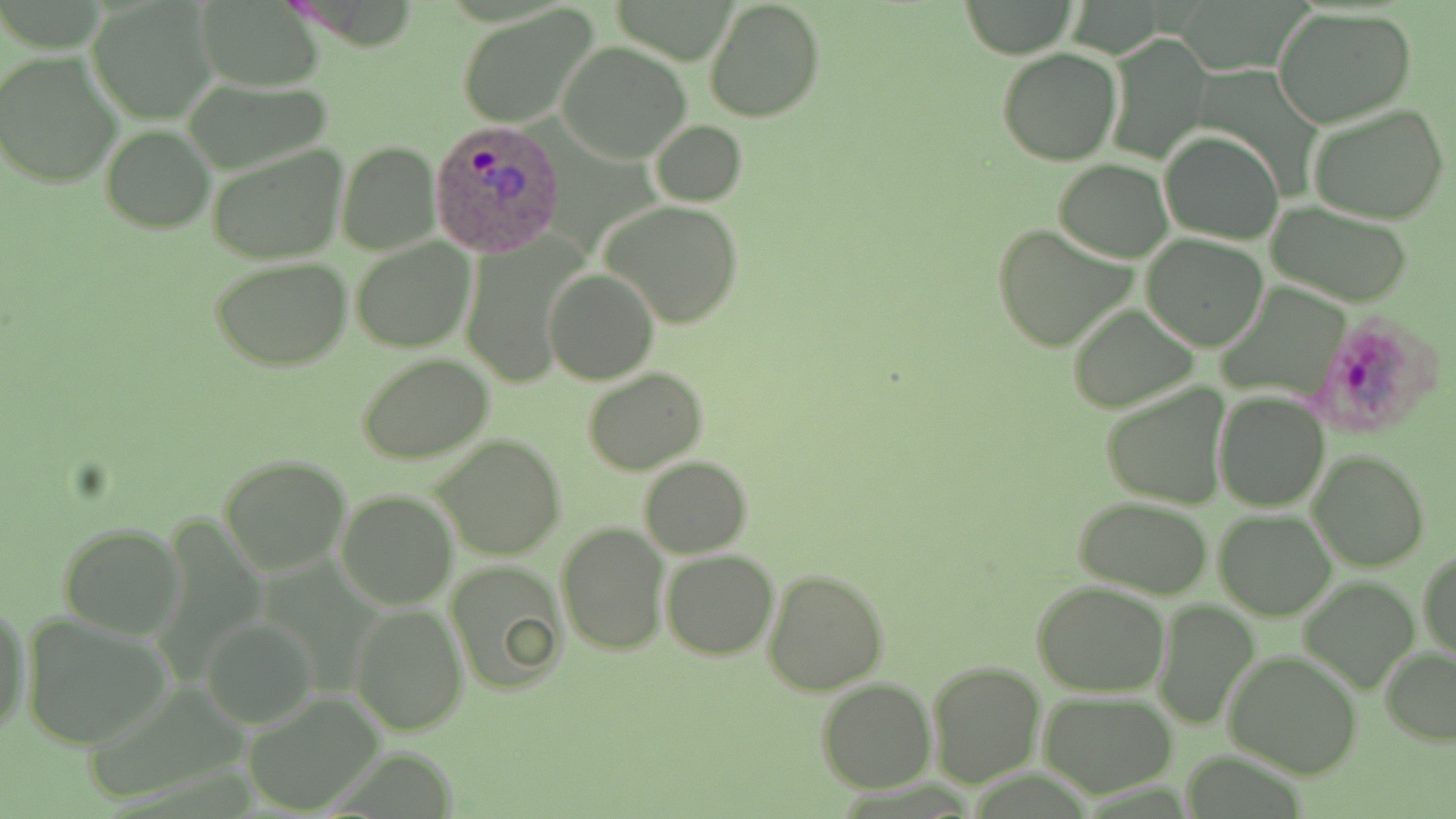
Summary:
  - Coordinate format: approximate bounding boxes as (x1,y1)-(x2,y2) corner pairs in pixels
  - Uninfected red blood cell locations: (87,0)-(219,122), (702,0)-(826,123), (193,1)-(328,90), (961,1)-(1077,58), (456,6)-(599,128), (1272,7)-(1417,128), (1103,33)-(1211,163), (558,41)-(694,165), (997,48)-(1121,165), (1,52)-(123,188), (183,76)-(339,177), (1308,103)-(1449,224), (649,119)-(747,206), (100,125)-(214,233), (1160,130)-(1284,244), (337,142)-(440,255), (206,145)-(349,263), (1055,159)-(1170,261), (336,167)-(450,323), (602,200)-(744,328), (1265,202)-(1415,306), (992,224)-(1138,353), (457,234)-(588,390), (1142,236)-(1270,351), (350,238)-(475,352), (209,256)-(354,370), (543,268)-(661,385), (1067,304)-(1199,414), (355,353)-(495,466), (582,365)-(708,475), (1103,385)-(1227,507), (1213,391)-(1329,512), (432,434)-(566,559), (1309,450)-(1431,572), (219,455)-(350,575), (639,457)-(752,558), (335,488)-(457,610), (1075,498)-(1213,599), (1213,509)-(1337,621), (556,522)-(668,655), (58,523)-(183,636), (662,548)-(779,660), (1418,548)-(1455,665), (444,560)-(568,695), (762,568)-(889,697), (1300,576)-(1420,694), (1033,580)-(1169,698), (1155,601)-(1259,731), (0,602)-(30,742), (350,605)-(468,735), (20,612)-(174,748), (203,618)-(317,731), (1380,647)-(1455,745), (1225,648)-(1364,778), (927,659)-(1046,786), (815,678)-(936,794), (1040,691)-(1179,798), (245,693)-(382,813)
  - Plasmodium ovale-infected red blood cell locations: (430,120)-(565,258), (1310,310)-(1446,440)
  - Slide-level diagnosis: Plasmodium ovale
  - Preparation: thin blood smear
  - Image size: 1456×819 pixels
  - Stain: May-Grünwald-Giemsa
  - Magnification: 1000x
  - Field of view: one of a larger specimen
  - Modality: optical microscopy